Locate every uninfected red blood cell.
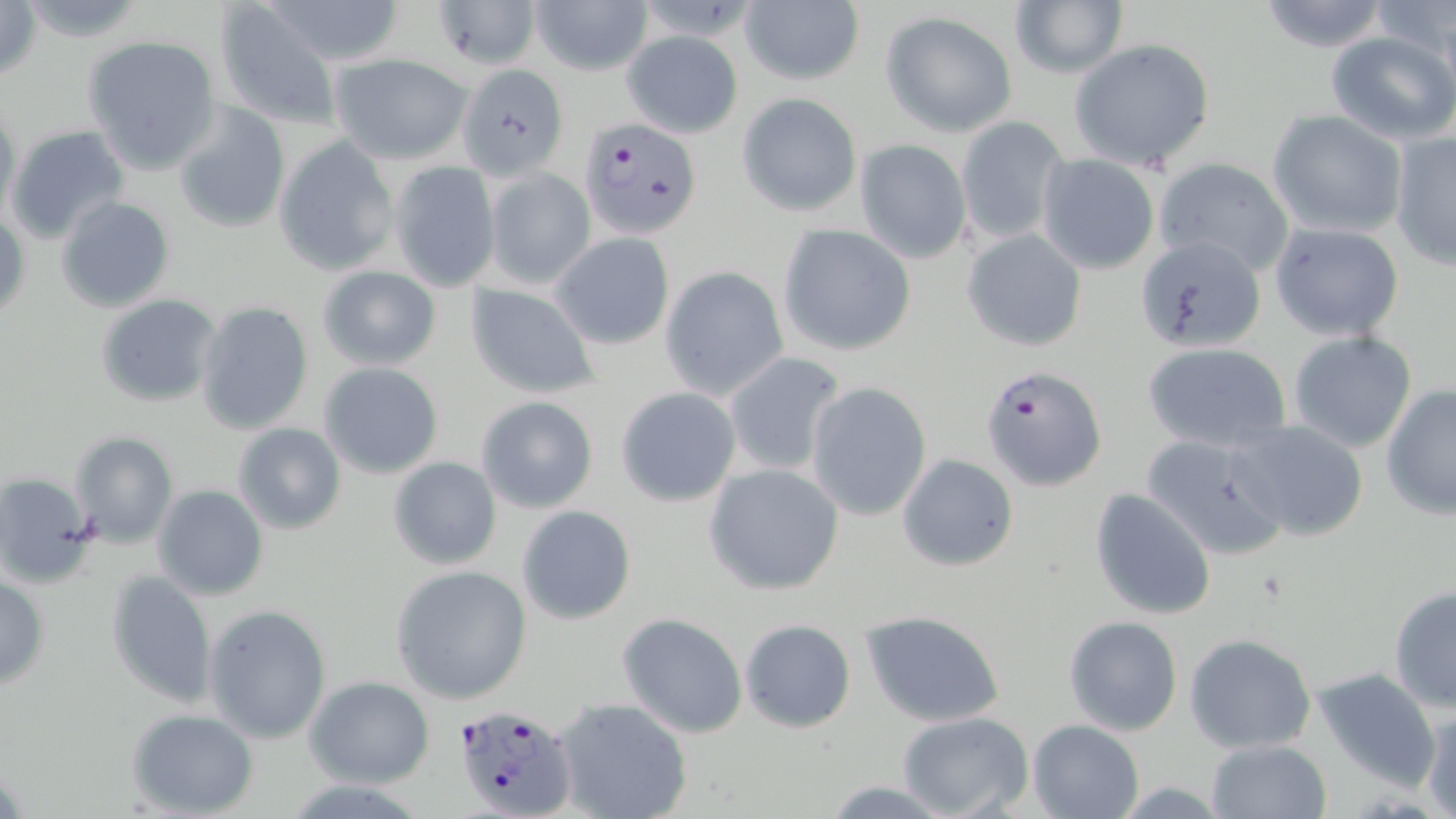
Approximate bounding boxes as [x1, y1, x2, y2] in pixels.
Uninfected red blood cells: [0, 0, 47, 79], [259, 0, 410, 66], [433, 0, 540, 71], [529, 0, 655, 77], [739, 0, 865, 86], [1254, 0, 1394, 53], [1010, 1, 1128, 79], [1369, 1, 1454, 62], [215, 4, 342, 129], [880, 11, 1017, 137], [621, 30, 743, 137], [1324, 31, 1456, 144], [82, 34, 223, 171], [1068, 38, 1215, 171], [330, 54, 471, 164], [458, 62, 568, 179], [737, 92, 863, 216], [175, 104, 291, 230], [0, 105, 21, 229], [1266, 109, 1408, 239], [955, 116, 1067, 247], [5, 123, 130, 246], [1389, 128, 1455, 271], [274, 136, 399, 275], [854, 139, 972, 265], [1037, 154, 1160, 274], [1153, 158, 1295, 276], [389, 161, 501, 290], [482, 165, 596, 289], [55, 195, 176, 313], [1, 208, 29, 327], [1269, 222, 1405, 340], [778, 225, 915, 355], [963, 230, 1087, 351], [550, 232, 676, 349], [1133, 234, 1268, 355], [317, 265, 442, 372], [659, 266, 788, 400], [465, 283, 601, 400], [94, 293, 220, 408], [194, 301, 315, 436], [1286, 330, 1419, 455], [1143, 342, 1292, 454], [721, 352, 847, 476], [319, 362, 445, 480], [805, 382, 932, 522], [1379, 383, 1456, 521], [614, 386, 742, 506], [476, 395, 598, 514], [1232, 419, 1369, 541], [231, 420, 347, 536], [68, 430, 179, 549], [1142, 434, 1289, 562], [897, 454, 1018, 570], [388, 455, 502, 570], [703, 463, 844, 596], [0, 471, 97, 588], [153, 484, 269, 600], [1089, 487, 1217, 621], [517, 505, 636, 624], [390, 563, 532, 704], [105, 568, 218, 710], [0, 575, 50, 691], [1388, 586, 1456, 713], [203, 604, 333, 744], [860, 610, 1006, 727], [618, 613, 748, 738], [1064, 616, 1182, 736], [738, 619, 856, 734], [1185, 633, 1317, 754], [1312, 666, 1441, 787], [305, 677, 435, 788], [554, 698, 693, 819], [1418, 706, 1456, 818], [126, 709, 258, 817], [898, 712, 1035, 819], [1027, 719, 1144, 819], [1206, 739, 1333, 819], [817, 780, 957, 816].

slide-level diagnosis = Plasmodium falciparum
modality = optical microscopy
stain = May-Grünwald-Giemsa
image size = 1456×819 pixels
Plasmodium falciparum-infected red blood cell locations = approximate bounding boxes as [x1, y1, x2, y2] in pixels: [578, 116, 701, 241], [982, 363, 1107, 493], [453, 703, 580, 819]
preparation = thin blood film
magnification = 1000x
field of view = single